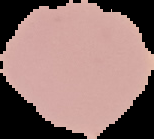

Summary:
  - Preparation: thin blood film
  - Image size: 154×139 pixels
  - Malaria status: uninfected
  - Image type: segmented cell region on a black background